Assess the morphology of the red blood cells.
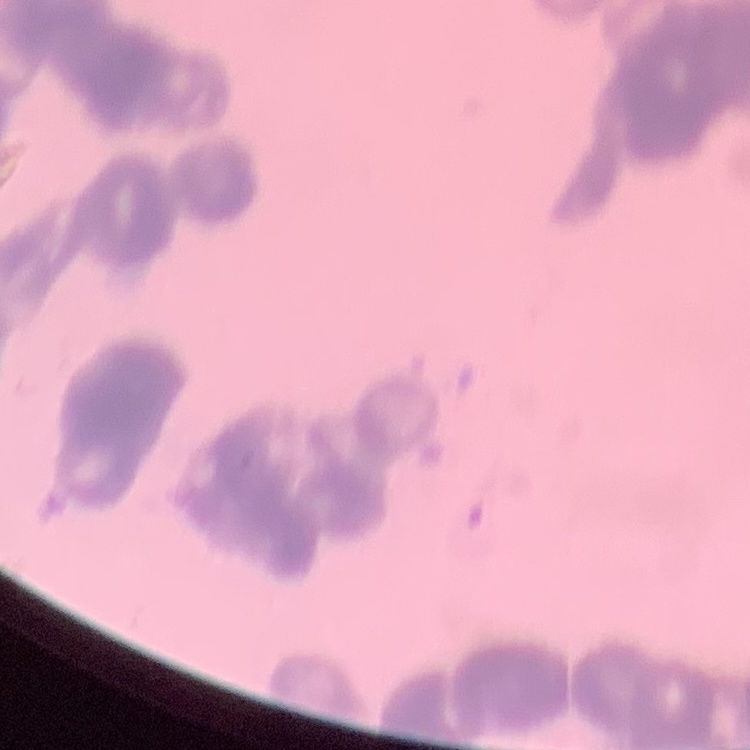

They show rouleaux formation.

Thin peripheral smear. One tile cut from a larger photomicrograph. Field's or Giemsa stain.